State the blood parasite species.
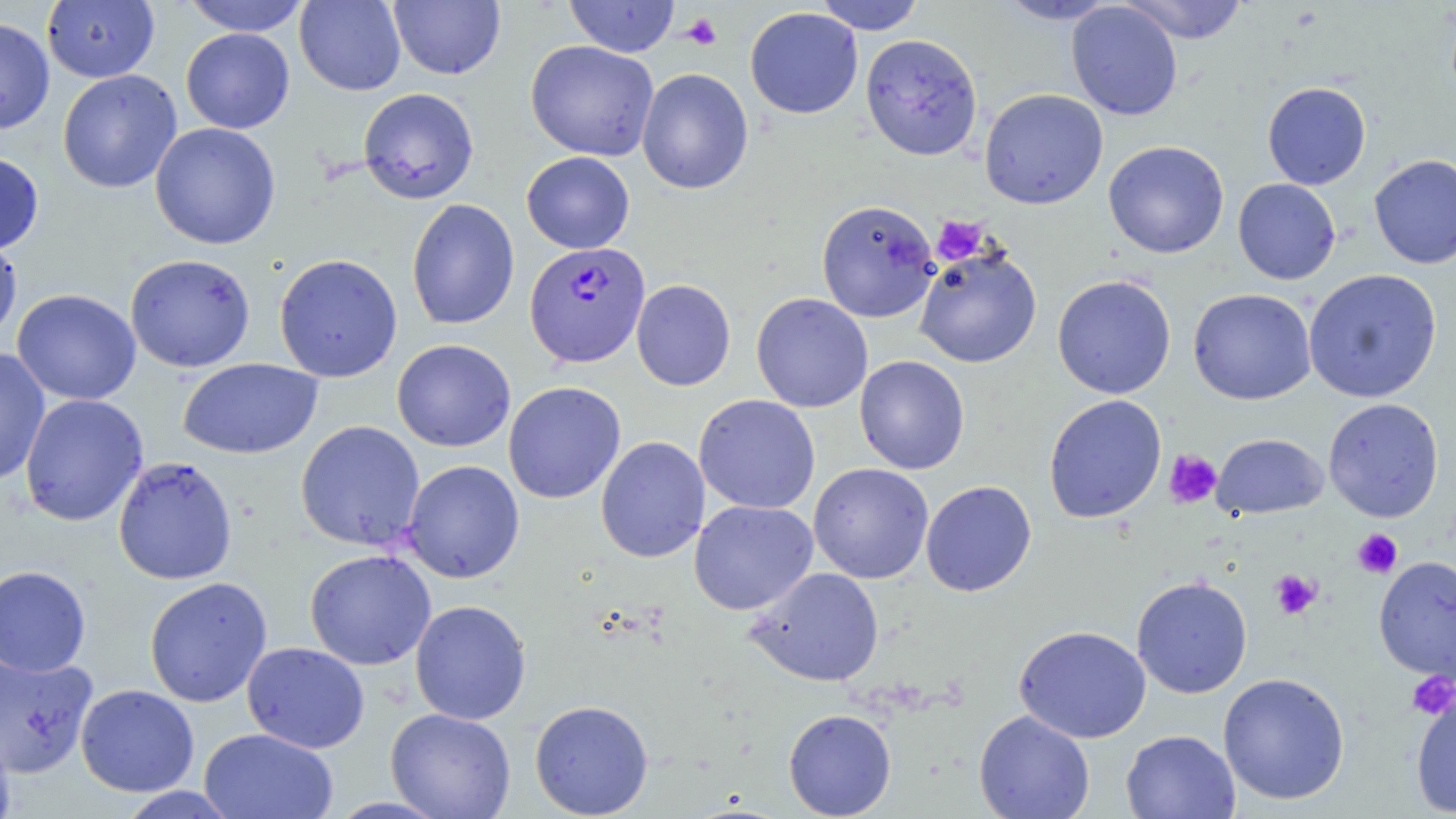
Plasmodium falciparum.

Approximate bounding boxes as named x1/y1/x2/y2 corners in pixels. Platelet locations: (x1=681, y1=13, x2=722, y2=50), (x1=932, y1=216, x2=989, y2=265), (x1=1163, y1=449, x2=1222, y2=509), (x1=1352, y1=529, x2=1402, y2=579), (x1=1269, y1=569, x2=1321, y2=620), (x1=1406, y1=672, x2=1455, y2=720). Plasmodium falciparum-infected red blood cell locations: (x1=525, y1=242, x2=651, y2=367). Uninfected red blood cell locations: (x1=181, y1=0, x2=311, y2=36), (x1=295, y1=0, x2=406, y2=95), (x1=389, y1=0, x2=505, y2=80), (x1=564, y1=0, x2=680, y2=57), (x1=814, y1=0, x2=926, y2=34), (x1=997, y1=0, x2=1120, y2=24), (x1=1118, y1=0, x2=1249, y2=44), (x1=42, y1=1, x2=160, y2=83), (x1=1067, y1=2, x2=1183, y2=120), (x1=745, y1=7, x2=863, y2=119), (x1=0, y1=17, x2=55, y2=134), (x1=181, y1=28, x2=295, y2=134), (x1=860, y1=33, x2=982, y2=160), (x1=525, y1=40, x2=659, y2=161), (x1=637, y1=68, x2=754, y2=194), (x1=57, y1=69, x2=182, y2=194), (x1=1262, y1=82, x2=1371, y2=189), (x1=358, y1=87, x2=479, y2=204), (x1=979, y1=88, x2=1108, y2=209), (x1=150, y1=122, x2=281, y2=249), (x1=1104, y1=140, x2=1229, y2=258), (x1=521, y1=151, x2=635, y2=253), (x1=0, y1=152, x2=44, y2=254), (x1=1369, y1=153, x2=1456, y2=269), (x1=1233, y1=178, x2=1340, y2=285), (x1=406, y1=198, x2=520, y2=330), (x1=816, y1=199, x2=941, y2=324), (x1=0, y1=232, x2=23, y2=345), (x1=914, y1=245, x2=1042, y2=368), (x1=125, y1=253, x2=255, y2=372), (x1=274, y1=253, x2=403, y2=382), (x1=1303, y1=268, x2=1442, y2=403), (x1=1052, y1=275, x2=1176, y2=399), (x1=631, y1=279, x2=736, y2=391), (x1=12, y1=288, x2=141, y2=405), (x1=1187, y1=288, x2=1317, y2=405), (x1=751, y1=293, x2=873, y2=413), (x1=392, y1=338, x2=515, y2=452), (x1=0, y1=348, x2=51, y2=486), (x1=854, y1=355, x2=970, y2=474), (x1=178, y1=358, x2=323, y2=459), (x1=503, y1=381, x2=626, y2=503), (x1=20, y1=394, x2=148, y2=526), (x1=693, y1=394, x2=821, y2=514), (x1=1043, y1=394, x2=1167, y2=523), (x1=1322, y1=398, x2=1444, y2=522), (x1=295, y1=420, x2=425, y2=551), (x1=1212, y1=433, x2=1328, y2=519), (x1=595, y1=435, x2=711, y2=563), (x1=113, y1=456, x2=238, y2=585), (x1=402, y1=459, x2=525, y2=583), (x1=808, y1=463, x2=933, y2=583), (x1=920, y1=480, x2=1037, y2=597), (x1=689, y1=499, x2=818, y2=615), (x1=304, y1=548, x2=436, y2=670), (x1=1374, y1=555, x2=1456, y2=681), (x1=0, y1=565, x2=91, y2=677), (x1=746, y1=567, x2=884, y2=687), (x1=144, y1=576, x2=273, y2=707), (x1=1131, y1=576, x2=1253, y2=698), (x1=410, y1=599, x2=531, y2=725), (x1=1014, y1=625, x2=1151, y2=743), (x1=242, y1=642, x2=370, y2=753), (x1=0, y1=652, x2=99, y2=777), (x1=1218, y1=672, x2=1350, y2=805), (x1=75, y1=684, x2=199, y2=797), (x1=1410, y1=684, x2=1456, y2=816), (x1=529, y1=699, x2=654, y2=817), (x1=385, y1=708, x2=516, y2=819), (x1=783, y1=708, x2=897, y2=818), (x1=974, y1=710, x2=1095, y2=819), (x1=0, y1=720, x2=16, y2=819), (x1=199, y1=727, x2=338, y2=819), (x1=1121, y1=729, x2=1240, y2=819), (x1=114, y1=787, x2=242, y2=818). Image is 1456×819 pixels. Light microscopy. 1000x magnification. Single field of view. May-Grünwald-Giemsa-stained preparation. Thin blood film.